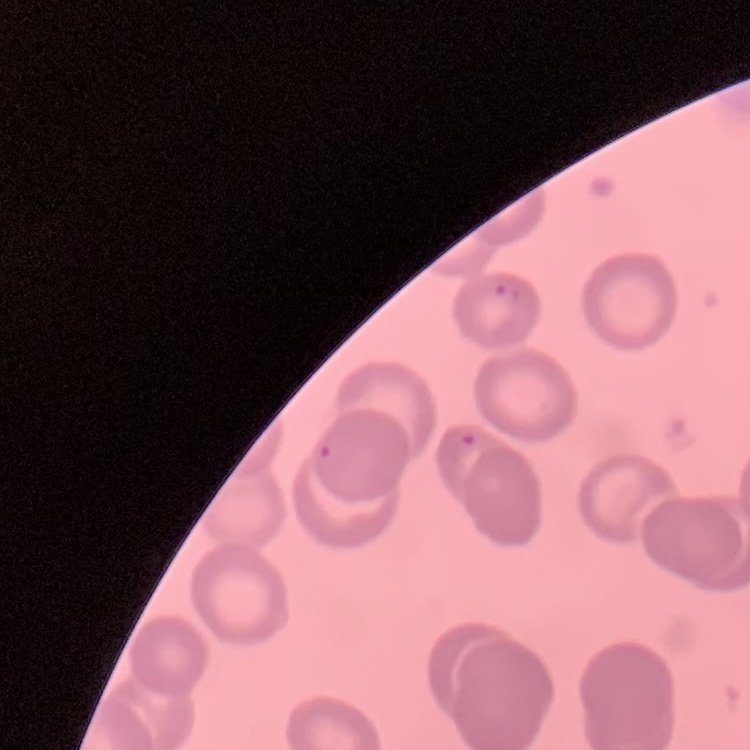

Summary:
  - Erythrocyte morphology: no rouleaux formation
  - Image type: one tile cut from a larger photomicrograph
  - Stain: Field's or Giemsa
  - Preparation: thin peripheral smear